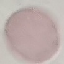

Result: no malaria parasites seen. Automatically extracted cell patch, resized to 64 × 64 pixels. Acquired by smartphone through the microscope eyepiece. Thin smear of blood. Giemsa-stained preparation.